Report the malaria status of this cell.
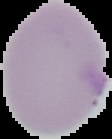
It is uninfected.

Image is 112×139 pixels. Segmented cell region on a black background. From a thin blood smear.